Assess this cell for malaria.
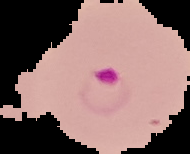
Parasitized.

Image is 190×154 pixels. Cell region segmented out of the field of view; the surrounding area is masked to black. From a thin blood film.